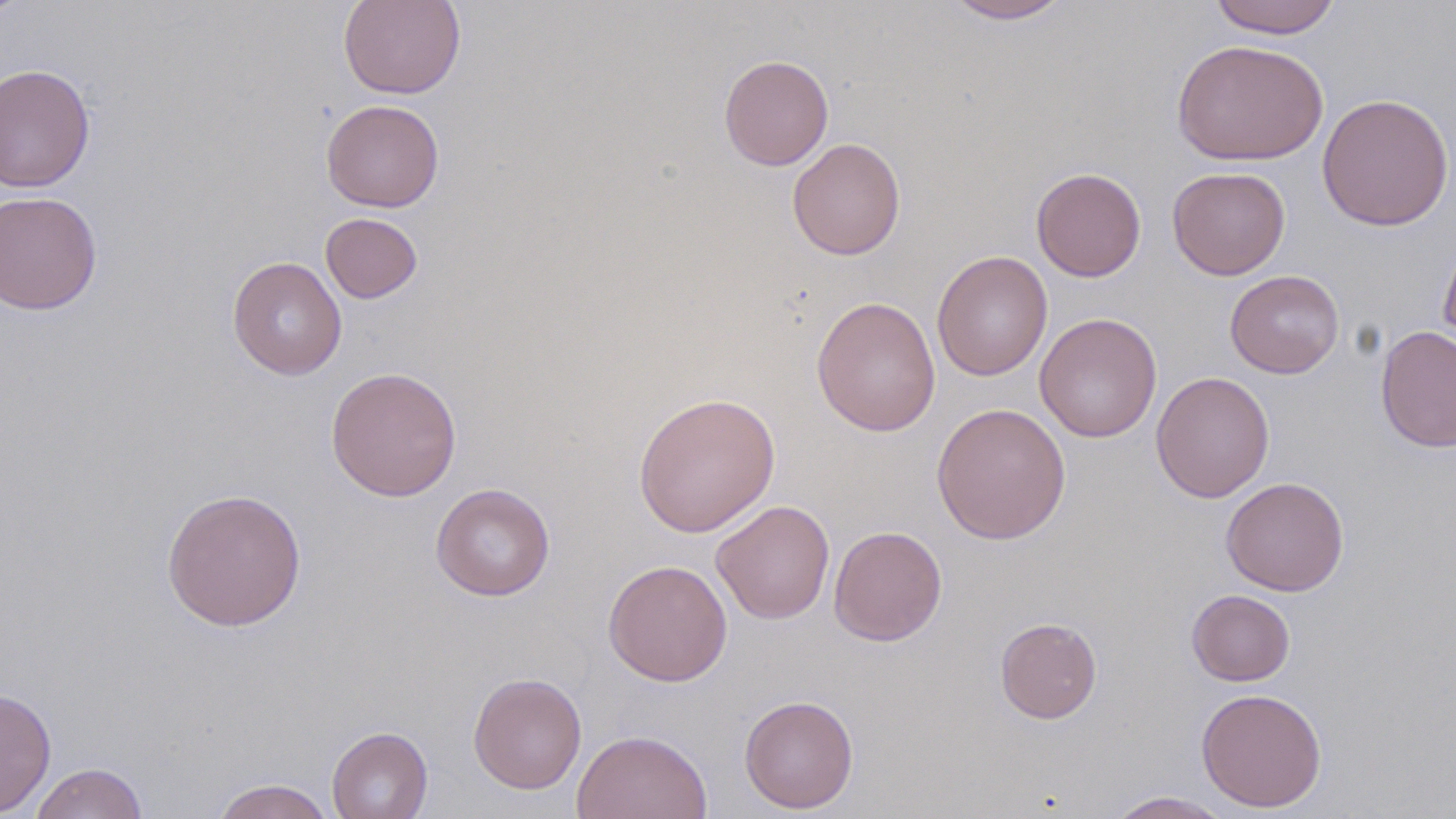

slide_level_diagnosis: no evidence of blood parasites
modality: optical microscopy
stain: May-Grünwald-Giemsa
field_of_view: one of a larger specimen
uninfected_red_blood_cell_locations: 'approximate bounding boxes as [x1, y1, x2, y2] in pixels: [0, 0, 26, 24], [338, 0, 465, 99], [939, 0, 1076, 24], [1208, 0, 1343, 38], [1171, 39, 1328, 166], [718, 54, 834, 170], [0, 63, 96, 193], [1316, 92, 1455, 232], [321, 99, 445, 212], [787, 138, 906, 260], [1031, 167, 1146, 282], [1167, 167, 1290, 280], [0, 190, 102, 315], [320, 212, 423, 304], [1438, 227, 1456, 355], [932, 250, 1052, 382], [226, 256, 347, 380], [1225, 270, 1345, 378], [811, 295, 941, 437], [1035, 313, 1163, 442], [1375, 325, 1456, 453], [325, 366, 463, 501], [1151, 371, 1275, 503], [632, 392, 781, 538], [930, 402, 1071, 545], [1220, 476, 1348, 596], [430, 483, 555, 601], [161, 488, 308, 631], [711, 500, 835, 624], [828, 525, 947, 646], [603, 559, 733, 686], [1186, 589, 1296, 686], [994, 616, 1102, 724], [468, 672, 587, 795], [0, 686, 57, 817], [1196, 687, 1327, 813], [739, 695, 859, 813], [327, 726, 433, 819], [571, 729, 713, 819], [28, 762, 148, 819], [211, 778, 337, 819], [1103, 791, 1235, 818]'
magnification: 1000x
image_size: 1456×819 pixels
preparation: thin blood smear